Name the blood parasite species.
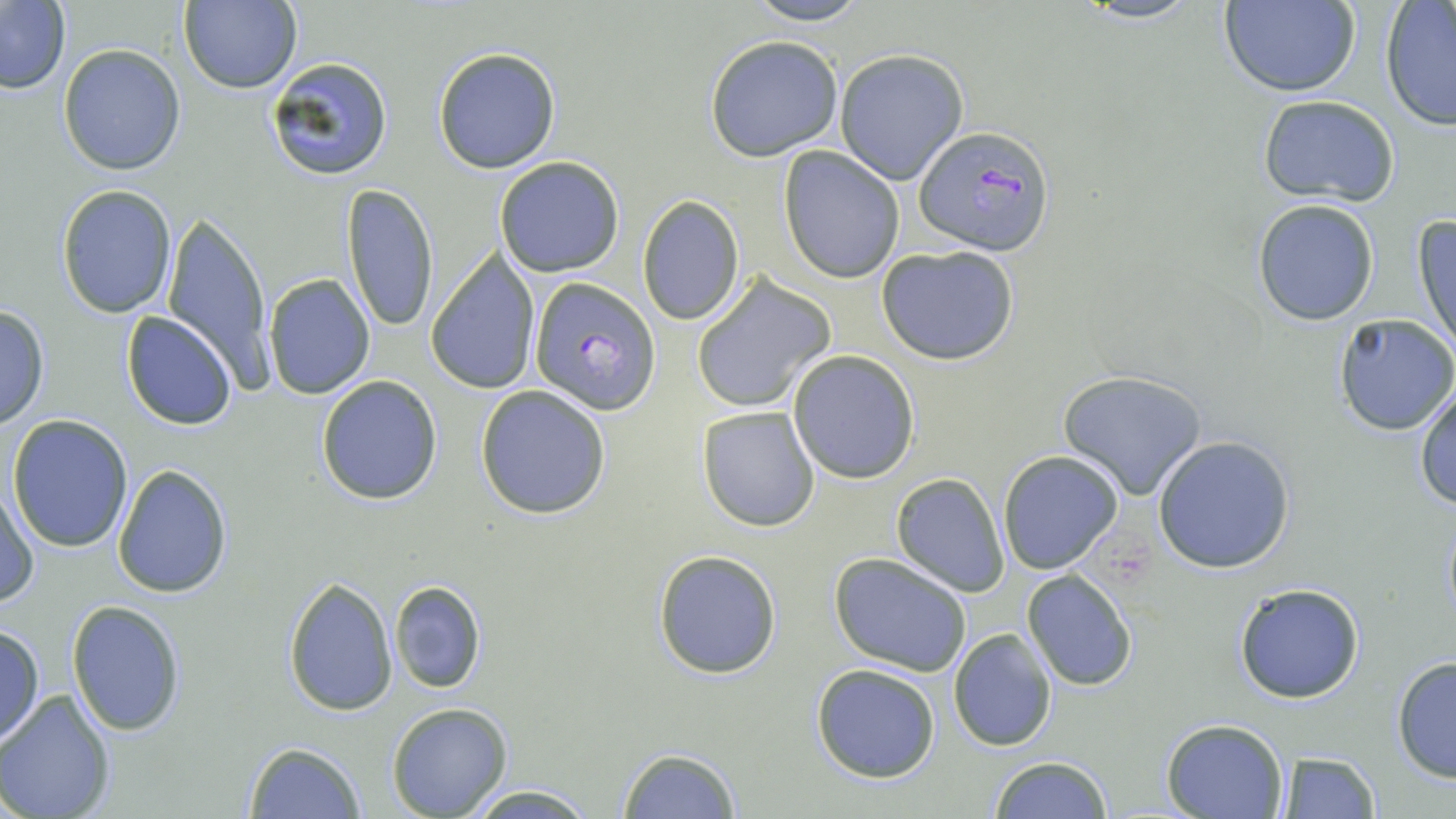
Plasmodium falciparum.

image_size: 1456×819 pixels
stain: May-Grünwald-Giemsa
field_of_view: single
preparation: thin blood film
modality: light microscopy
plasmodium_falciparum_infected_red_blood_cell_locations: 'approximate bounding boxes as (x1,y1)-(x2,y2) corner pairs in pixels: (913,125)-(1055,254), (528,278)-(659,414)'
uninfected_red_blood_cell_locations: 'approximate bounding boxes as (x1,y1)-(x2,y2) corner pairs in pixels: (177,0)-(302,93), (740,0)-(874,26), (1067,0)-(1209,25), (1217,1)-(1361,96), (0,2)-(72,93), (1380,3)-(1456,129), (704,35)-(843,161), (59,44)-(186,176), (432,46)-(562,174), (835,50)-(969,185), (266,56)-(394,182), (1256,96)-(1400,206), (779,147)-(904,284), (494,156)-(625,278), (339,182)-(440,334), (55,184)-(177,319), (636,195)-(746,326), (1252,200)-(1381,325), (158,212)-(278,392), (1413,214)-(1456,352), (876,244)-(1020,366), (426,252)-(541,394), (263,273)-(375,399), (691,275)-(835,413), (0,303)-(51,431), (121,310)-(237,431), (1332,313)-(1456,435), (788,350)-(920,483), (1057,369)-(1209,500), (315,374)-(443,505), (1411,381)-(1456,512), (476,384)-(612,520), (697,406)-(819,533), (6,415)-(132,552), (1152,435)-(1297,574), (997,448)-(1124,575), (111,464)-(233,598), (890,473)-(1011,597), (1,481)-(38,608), (1441,509)-(1456,630), (652,549)-(783,679), (827,552)-(974,677), (1022,569)-(1136,690), (281,577)-(396,717), (388,579)-(487,695), (1233,583)-(1365,703), (67,600)-(187,735), (0,625)-(45,746), (949,628)-(1059,750), (1390,656)-(1455,783), (810,662)-(942,784), (0,689)-(118,818), (386,702)-(514,818), (1161,717)-(1289,819), (243,741)-(365,818), (615,746)-(742,818), (1276,751)-(1382,818), (987,754)-(1114,818), (460,784)-(600,817)'
magnification: 1000x